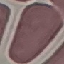

malaria status = uninfected
image type = automatically extracted cell patch, resized to 64 × 64 pixels
preparation = thin smear
stain = Giemsa
capture = smartphone through the microscope eyepiece